Assess for Plasmodium parasites.
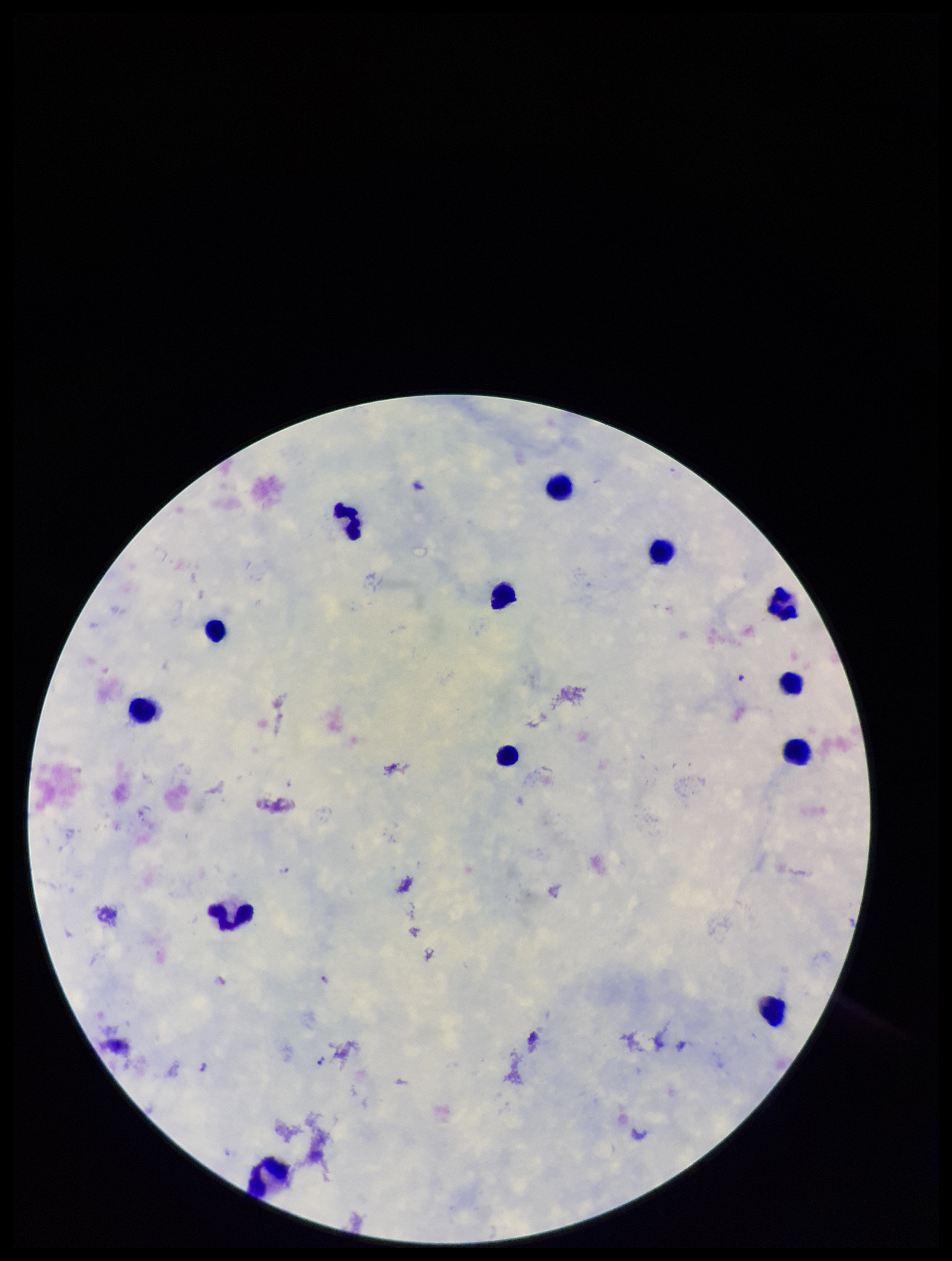
Identified.

field of view = one from this slide
patient malaria status = infected
image size = 952×1261 pixels
leukocyte count = 13
parasite count = 3
capture = smartphone photograph through the microscope eyepiece
preparation = thick smear
species reported for this patient = Plasmodium falciparum
stain = Giemsa